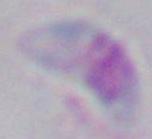

modality = photomicrograph
identification = Toxoplasma gondii
magnification = 1000x